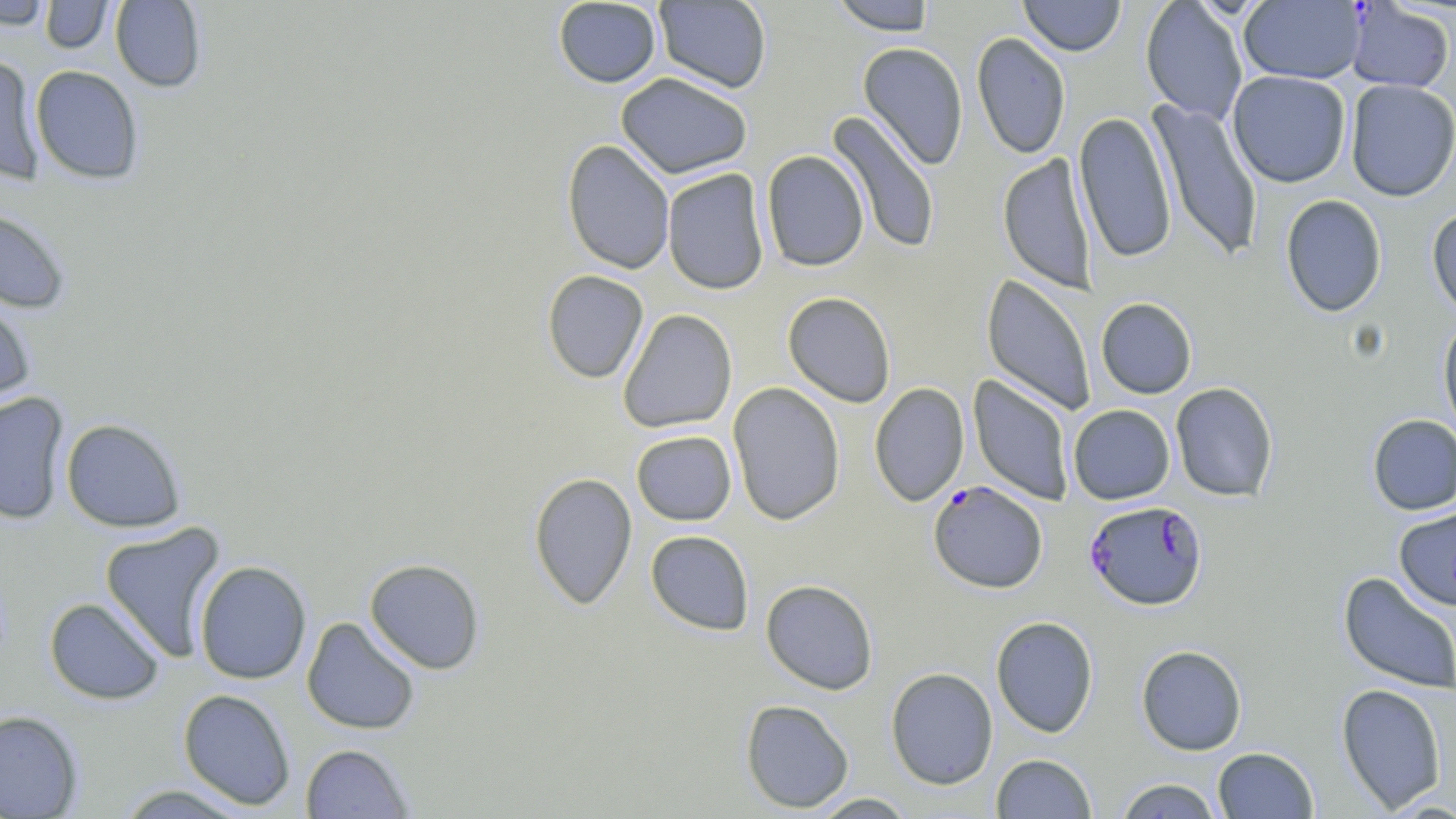
slide_level_diagnosis: Plasmodium falciparum
magnification: 1000x
field_of_view: one of a larger specimen
image_size: 1456×819 pixels
stain: May-Grünwald-Giemsa
preparation: thin blood smear
plasmodium_falciparum_infected_red_blood_cell_locations: 'approximate bounding boxes as named x1/y1/x2/y2 corners in pixels: (x1=928, y1=481, x2=1048, y2=594), (x1=1084, y1=500, x2=1208, y2=611)'
modality: optical microscopy
uninfected_red_blood_cell_locations: 'approximate bounding boxes as named x1/y1/x2/y2 corners in pixels: (x1=0, y1=0, x2=53, y2=29), (x1=41, y1=0, x2=115, y2=53), (x1=110, y1=0, x2=207, y2=92), (x1=553, y1=0, x2=661, y2=88), (x1=654, y1=0, x2=772, y2=93), (x1=829, y1=0, x2=936, y2=35), (x1=1019, y1=0, x2=1125, y2=56), (x1=1140, y1=1, x2=1248, y2=124), (x1=1238, y1=1, x2=1366, y2=84), (x1=1345, y1=2, x2=1454, y2=93), (x1=971, y1=31, x2=1071, y2=159), (x1=858, y1=42, x2=969, y2=170), (x1=0, y1=54, x2=45, y2=185), (x1=30, y1=65, x2=145, y2=184), (x1=1227, y1=71, x2=1351, y2=188), (x1=615, y1=72, x2=753, y2=179), (x1=1344, y1=79, x2=1456, y2=201), (x1=1149, y1=98, x2=1263, y2=263), (x1=1073, y1=110, x2=1176, y2=264), (x1=827, y1=111, x2=941, y2=255), (x1=561, y1=139, x2=675, y2=275), (x1=761, y1=150, x2=869, y2=272), (x1=998, y1=153, x2=1097, y2=293), (x1=662, y1=168, x2=769, y2=295), (x1=1279, y1=194, x2=1387, y2=318), (x1=0, y1=205, x2=72, y2=313), (x1=1427, y1=205, x2=1456, y2=322), (x1=542, y1=270, x2=649, y2=384), (x1=981, y1=273, x2=1096, y2=417), (x1=782, y1=291, x2=896, y2=408), (x1=0, y1=293, x2=36, y2=411), (x1=1096, y1=297, x2=1197, y2=399), (x1=618, y1=308, x2=737, y2=434), (x1=1438, y1=318, x2=1456, y2=442), (x1=968, y1=375, x2=1075, y2=506), (x1=728, y1=382, x2=846, y2=525), (x1=1170, y1=382, x2=1279, y2=502), (x1=869, y1=383, x2=969, y2=507), (x1=0, y1=392, x2=70, y2=525), (x1=1068, y1=404, x2=1175, y2=505), (x1=1367, y1=414, x2=1456, y2=515), (x1=61, y1=418, x2=186, y2=532), (x1=631, y1=430, x2=737, y2=526), (x1=528, y1=472, x2=637, y2=610), (x1=1394, y1=505, x2=1456, y2=611), (x1=99, y1=522, x2=226, y2=663), (x1=645, y1=530, x2=754, y2=635), (x1=364, y1=558, x2=485, y2=674), (x1=194, y1=560, x2=312, y2=684), (x1=1337, y1=571, x2=1456, y2=695), (x1=760, y1=579, x2=879, y2=695), (x1=44, y1=597, x2=165, y2=705), (x1=990, y1=616, x2=1099, y2=738), (x1=302, y1=617, x2=420, y2=734), (x1=1136, y1=645, x2=1247, y2=755), (x1=885, y1=667, x2=998, y2=790), (x1=1336, y1=683, x2=1449, y2=813), (x1=178, y1=688, x2=296, y2=810), (x1=740, y1=698, x2=855, y2=813), (x1=0, y1=710, x2=84, y2=818), (x1=300, y1=743, x2=415, y2=818), (x1=1213, y1=746, x2=1318, y2=818), (x1=991, y1=753, x2=1097, y2=818), (x1=1114, y1=778, x2=1223, y2=818), (x1=113, y1=784, x2=255, y2=818), (x1=808, y1=793, x2=917, y2=818)'